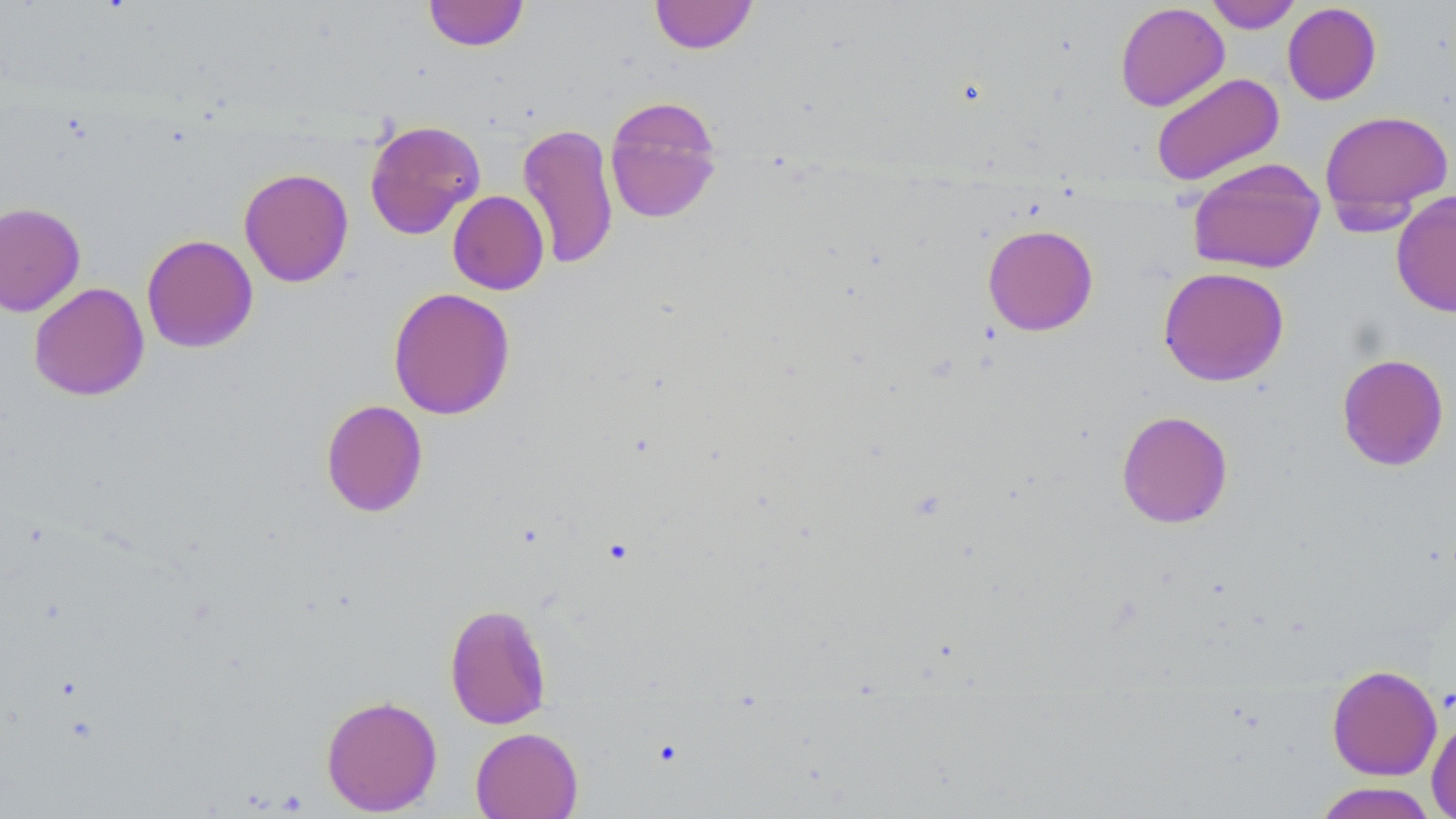

slide_level_diagnosis: negative for blood parasites
image_size: 1456×819 pixels
uninfected_red_blood_cell_locations: 'approximate bounding boxes as (x1,y1)-(x2,y2) corner pairs in pixels: (649,0)-(759,54), (1204,0)-(1302,33), (423,1)-(529,52), (1114,2)-(1230,112), (1282,3)-(1382,105), (1151,72)-(1285,187), (604,95)-(724,226), (1319,109)-(1454,223), (364,118)-(486,240), (517,122)-(620,270), (1187,158)-(1326,274), (238,168)-(354,287), (447,190)-(549,295), (1390,190)-(1456,318), (0,202)-(85,317), (982,224)-(1098,336), (141,234)-(259,353), (1158,266)-(1289,386), (28,282)-(149,401), (387,287)-(515,420), (1336,353)-(1450,471), (320,399)-(428,517), (1116,410)-(1233,528), (443,603)-(553,729), (1326,664)-(1442,780), (321,694)-(443,815), (1427,716)-(1456,819), (470,727)-(583,819), (1311,782)-(1441,819)'
magnification: 1000x
field_of_view: one of a larger specimen
modality: optical microscopy
preparation: thin blood smear
stain: May-Grünwald-Giemsa